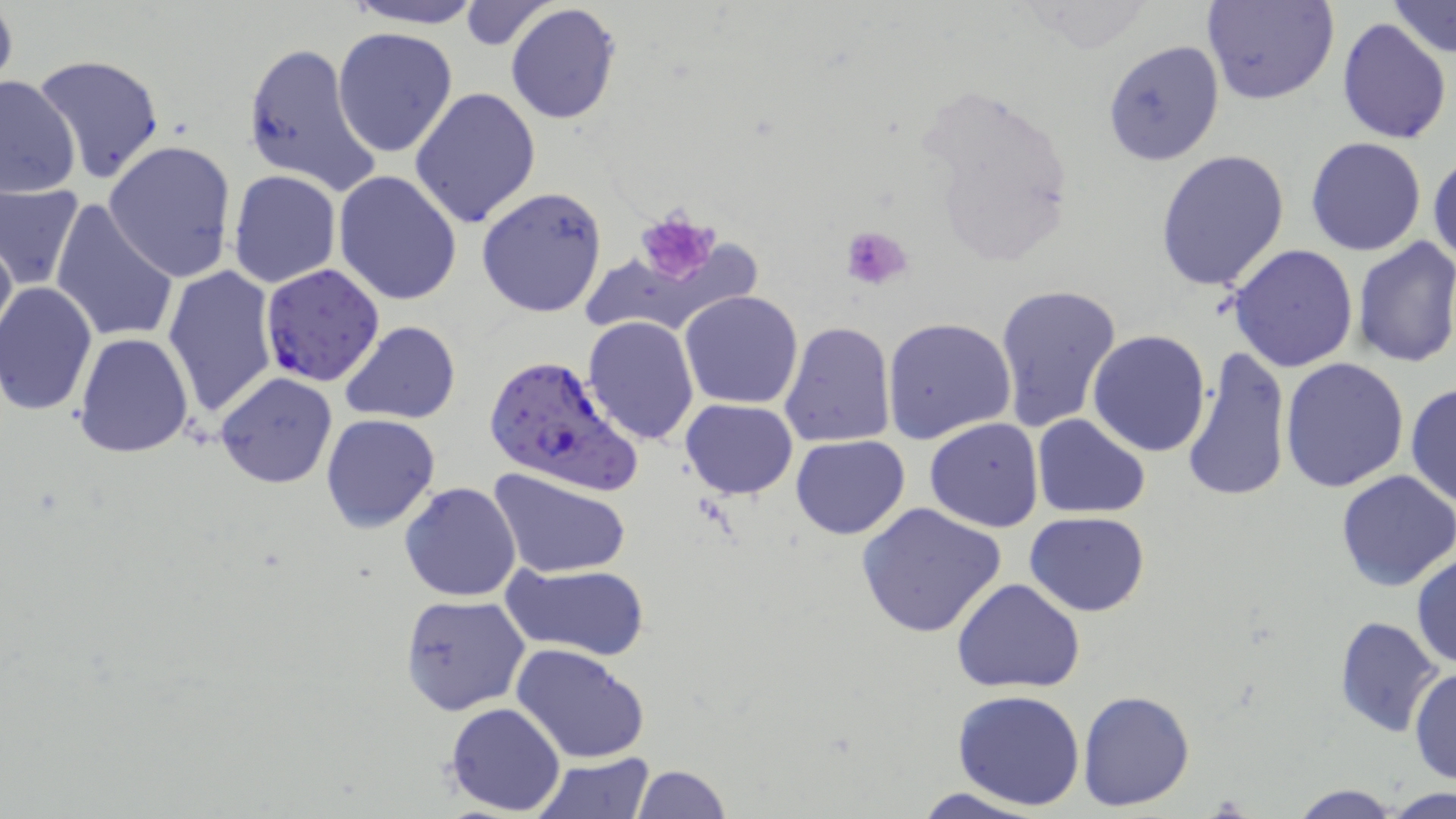
Summary:
  - Coordinate format: approximate bounding boxes as (x1, y1, x2, y2) in pixels
  - Plasmodium falciparum-infected red blood cell locations: (259, 265, 386, 388), (482, 354, 638, 493)
  - Uninfected red blood cell locations: (342, 0, 486, 29), (1202, 0, 1338, 105), (0, 1, 18, 99), (1388, 1, 1454, 60), (456, 2, 559, 50), (505, 3, 623, 126), (1336, 16, 1452, 144), (331, 27, 459, 159), (242, 40, 383, 198), (1101, 40, 1225, 167), (34, 55, 168, 185), (0, 72, 81, 197), (409, 87, 543, 232), (1304, 136, 1429, 256), (104, 140, 237, 283), (1156, 148, 1291, 293), (1429, 149, 1456, 272), (331, 169, 463, 306), (228, 170, 342, 290), (0, 182, 84, 292), (476, 185, 608, 319), (49, 200, 181, 344), (0, 224, 16, 349), (1352, 236, 1456, 370), (1228, 243, 1360, 372), (164, 265, 279, 423), (994, 281, 1122, 434), (0, 282, 98, 416), (679, 289, 802, 409), (582, 317, 701, 443), (883, 317, 1017, 446), (339, 320, 463, 424), (779, 320, 895, 449), (1087, 330, 1212, 458), (74, 333, 194, 458), (1180, 345, 1291, 505), (1279, 356, 1409, 493), (213, 372, 337, 490), (1405, 381, 1456, 513), (681, 399, 798, 499), (320, 413, 442, 534), (1032, 414, 1150, 518), (924, 418, 1044, 533), (790, 434, 910, 540), (490, 468, 631, 580), (1334, 470, 1456, 592), (399, 482, 522, 602), (855, 502, 1007, 638), (1024, 511, 1149, 615), (1410, 550, 1456, 670), (502, 562, 650, 661), (952, 578, 1086, 693), (400, 594, 529, 714), (1333, 616, 1443, 737), (511, 642, 650, 764), (458, 665, 617, 796), (1411, 666, 1455, 786), (953, 689, 1086, 810), (1077, 690, 1196, 810), (444, 703, 566, 816), (531, 754, 655, 817), (629, 764, 731, 818), (1287, 782, 1405, 818), (907, 785, 1051, 818), (1384, 786, 1453, 816)
  - Platelet locations: (636, 213, 720, 282), (839, 224, 913, 292)
  - Slide-level diagnosis: Plasmodium falciparum
  - Image size: 1456×819 pixels
  - Magnification: 1000x
  - Modality: optical microscopy
  - Stain: May-Grünwald-Giemsa
  - Preparation: thin blood smear
  - Field of view: single